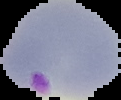
Image is 121×100 pixels. Segmented cell region on a black background. Malaria status: parasitized. From a thin blood film.